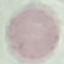
Summary:
  - Malaria status: uninfected
  - Capture: smartphone camera at the microscope eyepiece
  - Preparation: thin smear
  - Image type: automatically extracted cell patch, resized to 64 × 64 pixels
  - Stain: Giemsa